Name the blood parasite species.
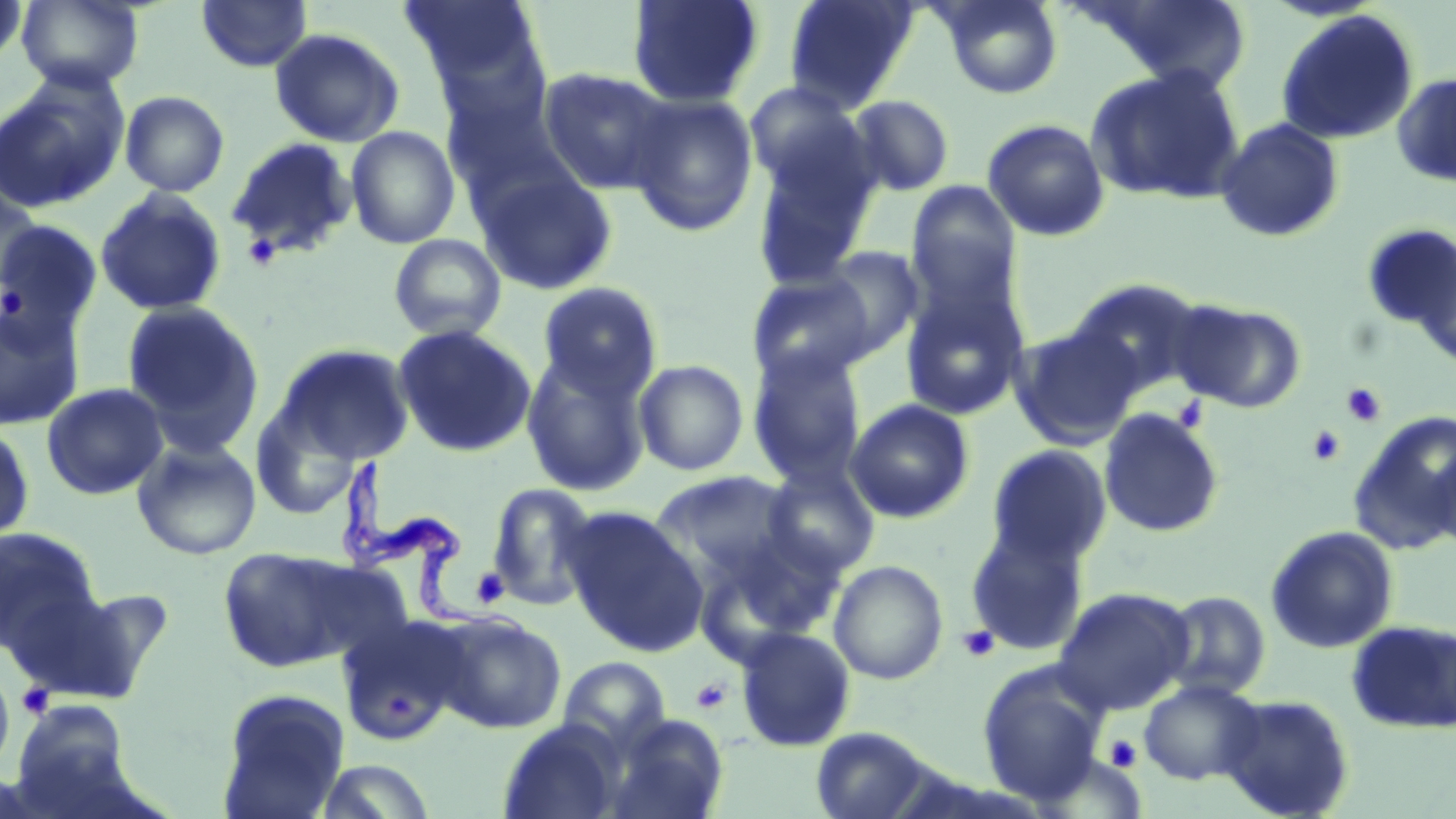
Trypanosoma brucei.

stain = May-Grünwald-Giemsa
Trypanosoma brucei locations = approximate bounding boxes as named x1/y1/x2/y2 corners in pixels: (x1=339, y1=462, x2=526, y2=638)
magnification = 1000x
image size = 1456×819 pixels
platelet locations = approximate bounding boxes as named x1/y1/x2/y2 corners in pixels: (x1=240, y1=232, x2=283, y2=272), (x1=1341, y1=383, x2=1387, y2=427), (x1=1172, y1=395, x2=1210, y2=435), (x1=1307, y1=425, x2=1346, y2=466), (x1=471, y1=567, x2=510, y2=609), (x1=957, y1=625, x2=1000, y2=662), (x1=691, y1=678, x2=732, y2=714), (x1=16, y1=683, x2=54, y2=719), (x1=1104, y1=734, x2=1143, y2=773)
uninfected red blood cell locations = approximate bounding boxes as named x1/y1/x2/y2 corners in pixels: (x1=0, y1=0, x2=29, y2=71), (x1=16, y1=0, x2=144, y2=91), (x1=196, y1=0, x2=312, y2=72), (x1=398, y1=0, x2=544, y2=92), (x1=783, y1=0, x2=919, y2=112), (x1=935, y1=0, x2=1064, y2=99), (x1=1083, y1=0, x2=1254, y2=94), (x1=626, y1=1, x2=765, y2=108), (x1=1275, y1=8, x2=1420, y2=146), (x1=269, y1=27, x2=405, y2=148), (x1=537, y1=66, x2=674, y2=195), (x1=1085, y1=66, x2=1246, y2=203), (x1=1391, y1=71, x2=1456, y2=188), (x1=0, y1=76, x2=128, y2=212), (x1=744, y1=81, x2=869, y2=197), (x1=441, y1=86, x2=577, y2=210), (x1=119, y1=90, x2=230, y2=197), (x1=625, y1=93, x2=759, y2=237), (x1=846, y1=94, x2=954, y2=197), (x1=1215, y1=117, x2=1345, y2=243), (x1=982, y1=118, x2=1110, y2=241), (x1=345, y1=125, x2=461, y2=249), (x1=226, y1=137, x2=359, y2=261), (x1=749, y1=139, x2=880, y2=289), (x1=476, y1=167, x2=619, y2=296), (x1=905, y1=181, x2=1022, y2=310), (x1=0, y1=182, x2=47, y2=297), (x1=95, y1=188, x2=227, y2=316), (x1=0, y1=218, x2=103, y2=347), (x1=1361, y1=222, x2=1456, y2=348), (x1=388, y1=233, x2=508, y2=342), (x1=815, y1=247, x2=924, y2=360), (x1=746, y1=271, x2=877, y2=388), (x1=899, y1=272, x2=1031, y2=421), (x1=1068, y1=277, x2=1208, y2=397), (x1=536, y1=282, x2=664, y2=401), (x1=121, y1=299, x2=265, y2=455), (x1=1171, y1=299, x2=1307, y2=412), (x1=1, y1=300, x2=84, y2=432), (x1=393, y1=324, x2=537, y2=457), (x1=1010, y1=325, x2=1141, y2=450), (x1=274, y1=343, x2=415, y2=465), (x1=747, y1=346, x2=867, y2=487), (x1=521, y1=353, x2=653, y2=495), (x1=633, y1=359, x2=749, y2=476), (x1=41, y1=382, x2=168, y2=501), (x1=845, y1=398, x2=975, y2=524), (x1=250, y1=400, x2=361, y2=522), (x1=1098, y1=408, x2=1225, y2=539), (x1=1349, y1=410, x2=1456, y2=555), (x1=0, y1=422, x2=36, y2=546), (x1=131, y1=438, x2=262, y2=560), (x1=1429, y1=440, x2=1456, y2=556), (x1=986, y1=444, x2=1112, y2=566), (x1=760, y1=464, x2=879, y2=578), (x1=650, y1=471, x2=802, y2=588), (x1=485, y1=482, x2=601, y2=610), (x1=563, y1=507, x2=707, y2=653), (x1=965, y1=522, x2=1090, y2=656), (x1=698, y1=525, x2=848, y2=651), (x1=1264, y1=525, x2=1398, y2=653), (x1=0, y1=526, x2=101, y2=653), (x1=217, y1=545, x2=366, y2=673), (x1=828, y1=560, x2=948, y2=685), (x1=5, y1=581, x2=155, y2=703), (x1=1053, y1=587, x2=1194, y2=714), (x1=1161, y1=591, x2=1271, y2=700), (x1=433, y1=612, x2=566, y2=734), (x1=337, y1=618, x2=465, y2=747), (x1=1347, y1=620, x2=1456, y2=734), (x1=735, y1=627, x2=856, y2=752), (x1=557, y1=656, x2=670, y2=751), (x1=977, y1=661, x2=1111, y2=805), (x1=0, y1=671, x2=15, y2=772), (x1=1138, y1=679, x2=1264, y2=785), (x1=216, y1=687, x2=351, y2=818), (x1=1218, y1=693, x2=1356, y2=818), (x1=13, y1=700, x2=132, y2=805), (x1=601, y1=712, x2=729, y2=819), (x1=497, y1=718, x2=627, y2=819), (x1=809, y1=725, x2=938, y2=819), (x1=312, y1=759, x2=437, y2=818)
preparation = thin blood smear
field of view = one of a larger specimen
modality = optical microscopy